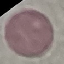
result = negative for malaria parasites
preparation = thin smear
image type = cell patch, automatically extracted from a larger field of view and resized to 64 × 64 pixels
stain = Giemsa
capture = smartphone through the microscope eyepiece